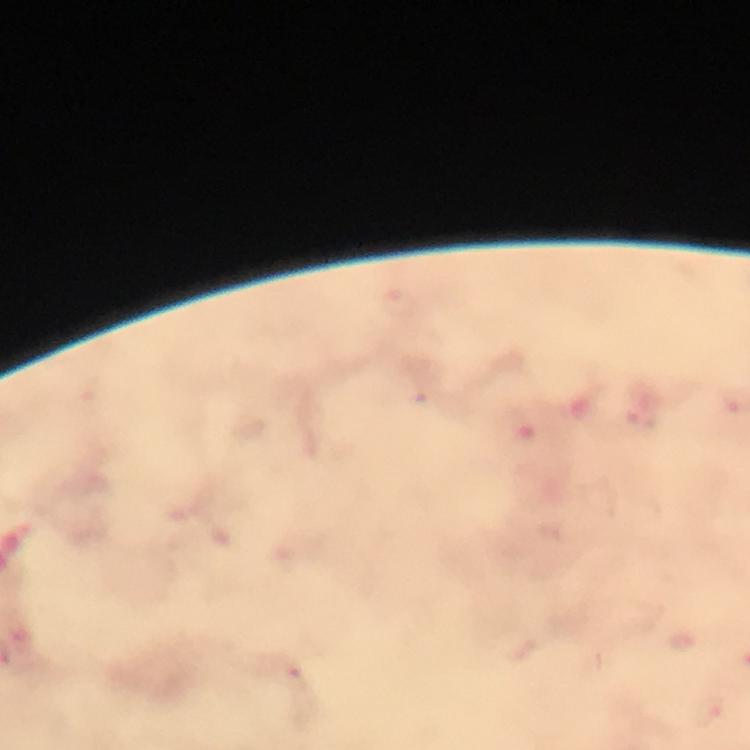
Approximate centers as [x, y] in pixels. Malaria parasite locations: [295, 677]. Photographed with a smartphone mounted on the microscope. 100x magnification. Thick blood film. Image is 750×750 pixels. Immersion oil applied. Giemsa stain. Cropped region of a single field of view. From a malaria diagnostic workup.